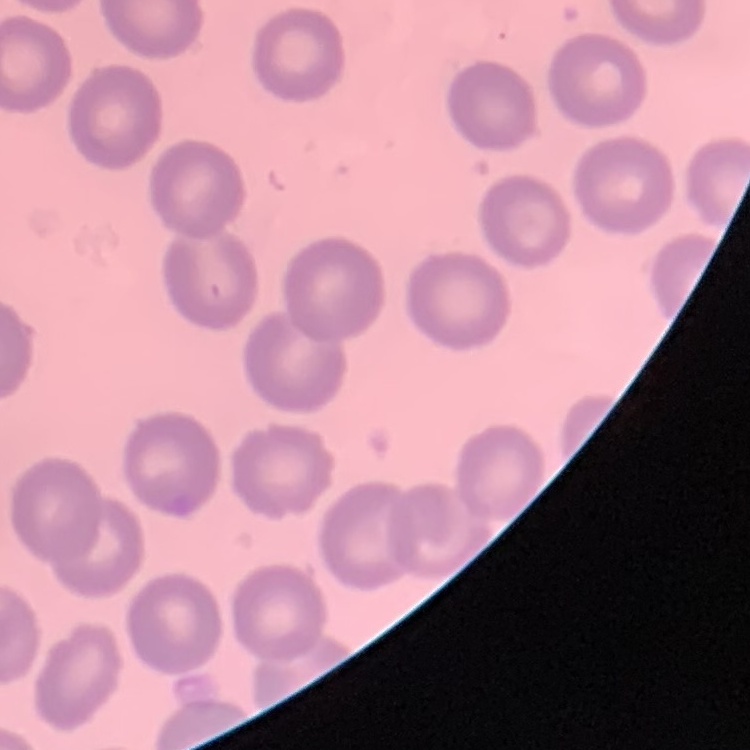 The red blood cells show no rouleaux formation. Thin blood smear. Field's or Giemsa stain. Square crop of a larger photomicrograph.